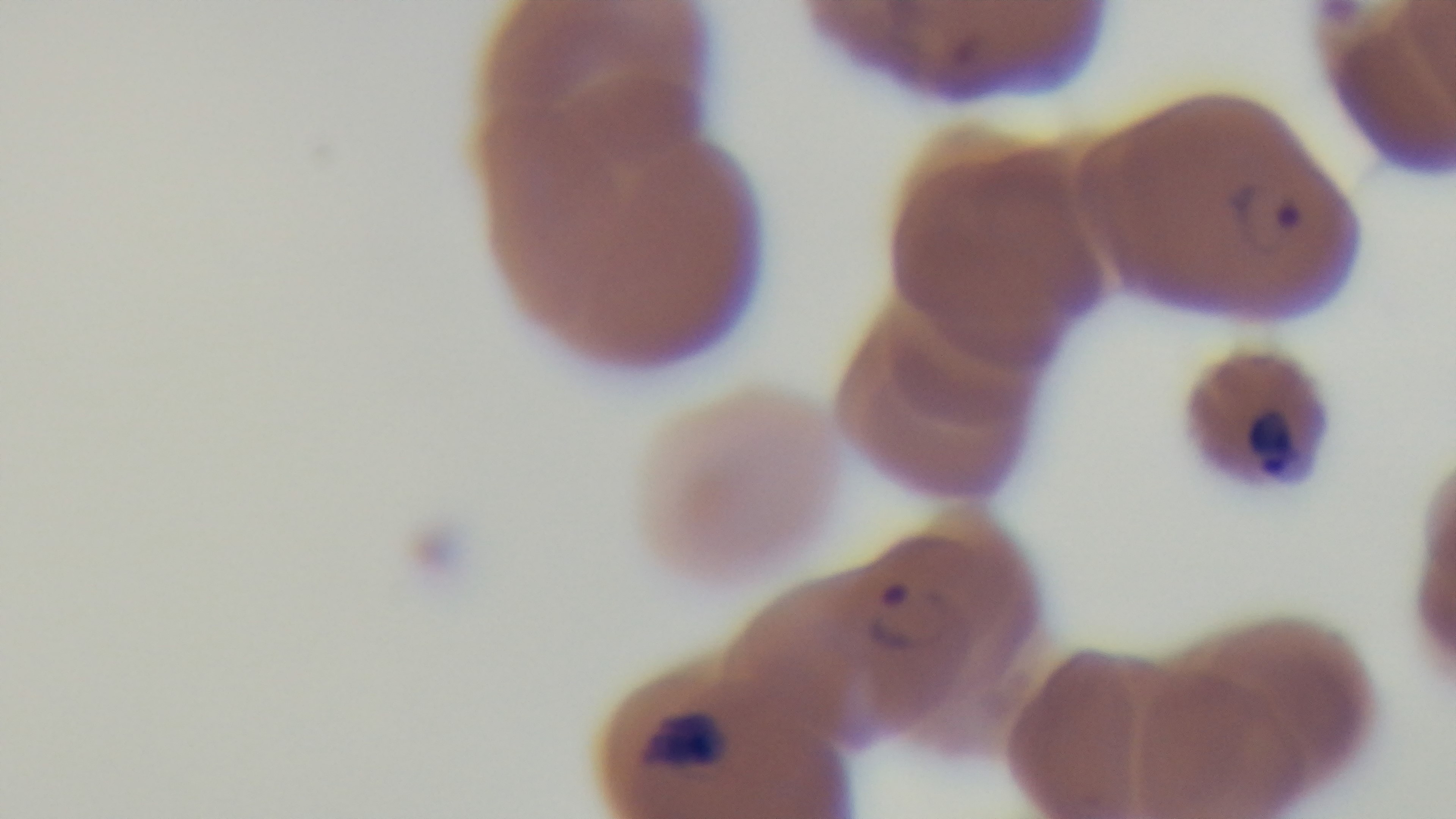
Summary:
  - Stain: Giemsa
  - Field of view: one from the slide
  - Malaria status: positive
  - Capture: mounted 4K digital camera
  - Modality: light microscopy
  - Objective: 100x oil immersion
  - Preparation: thin